Report the malaria status of this cell.
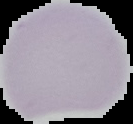

Uninfected.

From a thin blood smear. Cell region segmented out of the field of view; the surrounding area is masked to black. Image is 133×124 pixels.